Assess this cell for malaria.
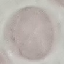
It is uninfected.

Giemsa stain. Cell patch, automatically extracted from a larger field of view and resized to 64 × 64 pixels. Thin blood film. Photographed with a smartphone camera at the microscope eyepiece.